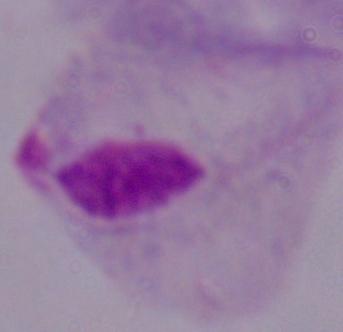
Summary:
  - Magnification: 1000x
  - Modality: photomicrograph
  - Identification: trichomonad